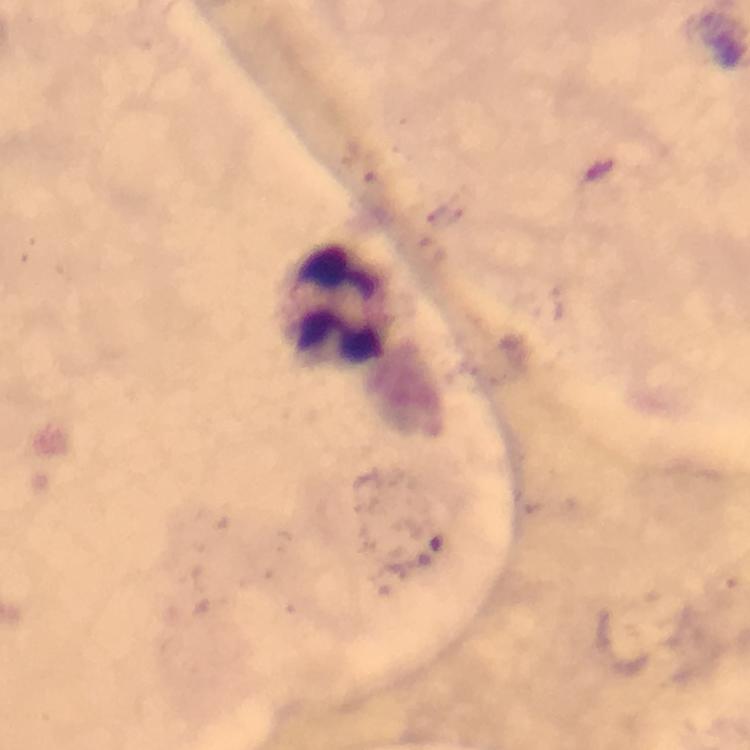 Approximate object centers, in pixels from the top-left corner. Leukocyte locations: (x=337, y=304). Smartphone photograph taken through a microscope. From a diagnostic examination for malaria. Image is 750×750 pixels. Immersion oil applied. At 100x magnification. Plasmodium parasites: none detected. Giemsa stain. Thick smear. Cropped region of a single field of view.